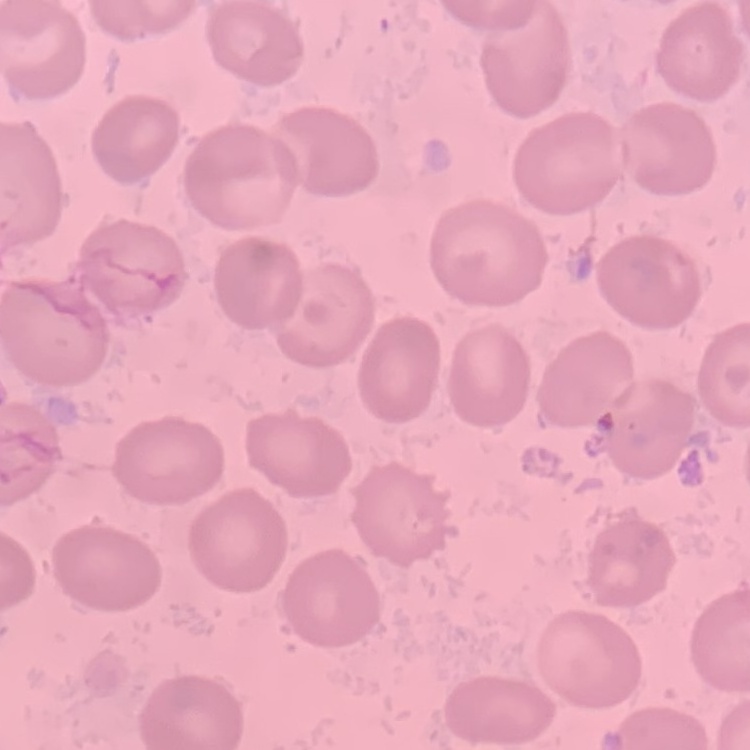
{
  "erythrocyte_morphology": "no rouleaux formation",
  "preparation": "thin blood film",
  "image_type": "one tile cut from a larger photomicrograph",
  "stain": "Field's or Giemsa"
}